Identify the blood parasite species.
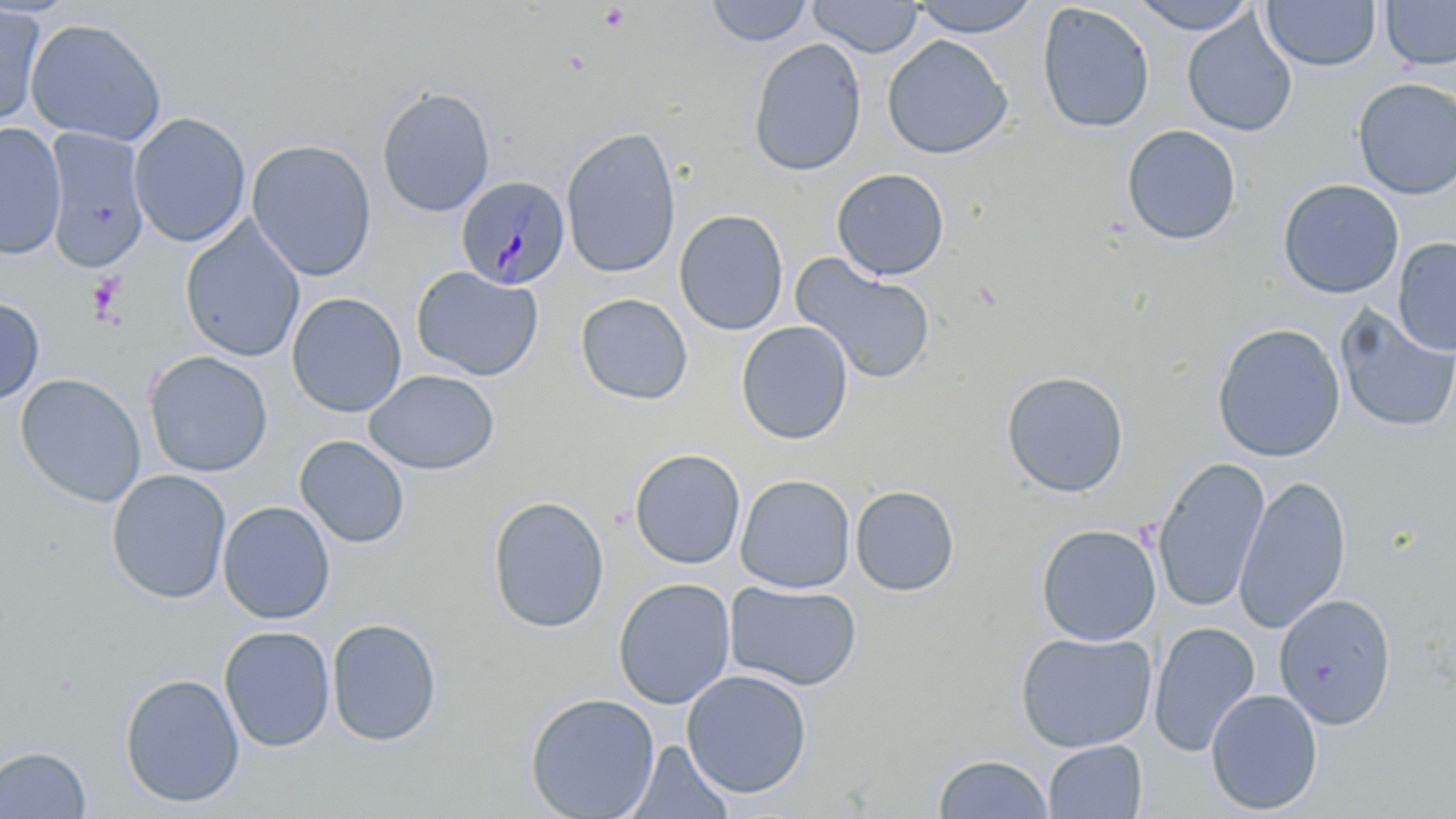

Plasmodium malariae.

Approximate bounding boxes as [x1, y1, x2, y2] in pixels. Platelet locations: [598, 3, 630, 31], [88, 273, 125, 321]. Uninfected red blood cell locations: [706, 0, 814, 48], [1130, 0, 1261, 35], [808, 1, 923, 58], [907, 1, 1043, 38], [1262, 1, 1381, 71], [1380, 1, 1456, 70], [1036, 3, 1156, 134], [0, 4, 45, 128], [1182, 13, 1297, 138], [25, 17, 167, 146], [882, 35, 1013, 160], [748, 37, 868, 177], [1352, 78, 1456, 199], [376, 87, 495, 217], [128, 112, 251, 248], [0, 123, 66, 260], [1121, 124, 1242, 245], [560, 126, 682, 278], [43, 127, 150, 272], [246, 139, 377, 282], [831, 168, 950, 281], [1277, 179, 1405, 299], [675, 209, 789, 335], [180, 219, 305, 362], [1393, 237, 1456, 357], [790, 253, 938, 386], [410, 266, 544, 381], [286, 292, 407, 417], [575, 293, 693, 406], [0, 297, 44, 406], [1333, 305, 1456, 434], [736, 320, 854, 445], [1211, 323, 1346, 463], [144, 350, 273, 477], [364, 369, 500, 476], [1001, 370, 1130, 498], [16, 373, 146, 507], [294, 435, 410, 549], [629, 448, 746, 570], [1152, 457, 1270, 614], [106, 468, 232, 604], [735, 474, 856, 593], [1234, 474, 1351, 634], [850, 485, 960, 596], [487, 495, 610, 634], [218, 500, 335, 625], [1035, 523, 1161, 646], [613, 577, 737, 709], [725, 580, 863, 692], [1274, 593, 1397, 729], [326, 617, 443, 747], [1148, 621, 1261, 756], [219, 625, 335, 752], [1015, 630, 1158, 753], [681, 669, 813, 798], [120, 673, 245, 808], [1205, 688, 1323, 815], [524, 692, 660, 819], [1042, 739, 1147, 819], [625, 740, 735, 819], [0, 745, 92, 818], [932, 753, 1053, 818]. Plasmodium malariae-infected red blood cell locations: [456, 175, 571, 289]. Optical microscopy. Thin blood smear. Single field of view. May-Grünwald-Giemsa-stained preparation. Image is 1456×819 pixels. 1000x magnification.